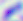
identification = Toxoplasma gondii
modality = photomicrograph
magnification = 400x